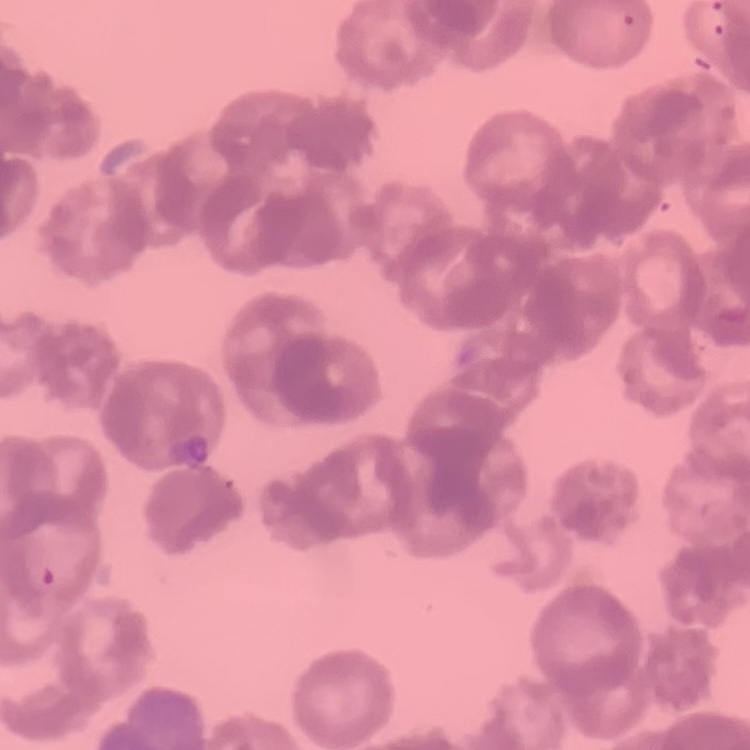
Summary:
  - Red blood cell morphology: rouleaux formation
  - Stain: Field's or Giemsa
  - Preparation: thin peripheral smear
  - Image type: one tile cut from a larger photomicrograph